State which parasite is depicted.
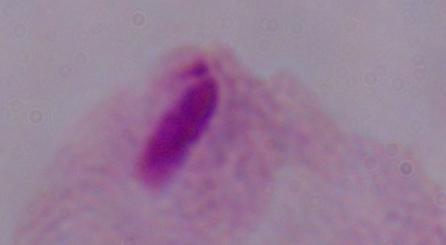
A trichomonad.

modality = photomicrograph
magnification = 1000x